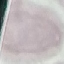

Result: negative for malaria parasites. Thin smear of blood. Cell patch, automatically extracted from a larger field of view and resized to 64 × 64 pixels. Acquired by smartphone through the microscope eyepiece. Giemsa stain.